Assess this cell for malaria.
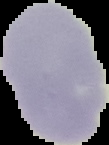

Uninfected.

{
  "preparation": "thin blood smear",
  "image_size": "109×145 pixels",
  "image_type": "segmented cell region on a black background"
}